Give the extent of all uninfected red blood cells.
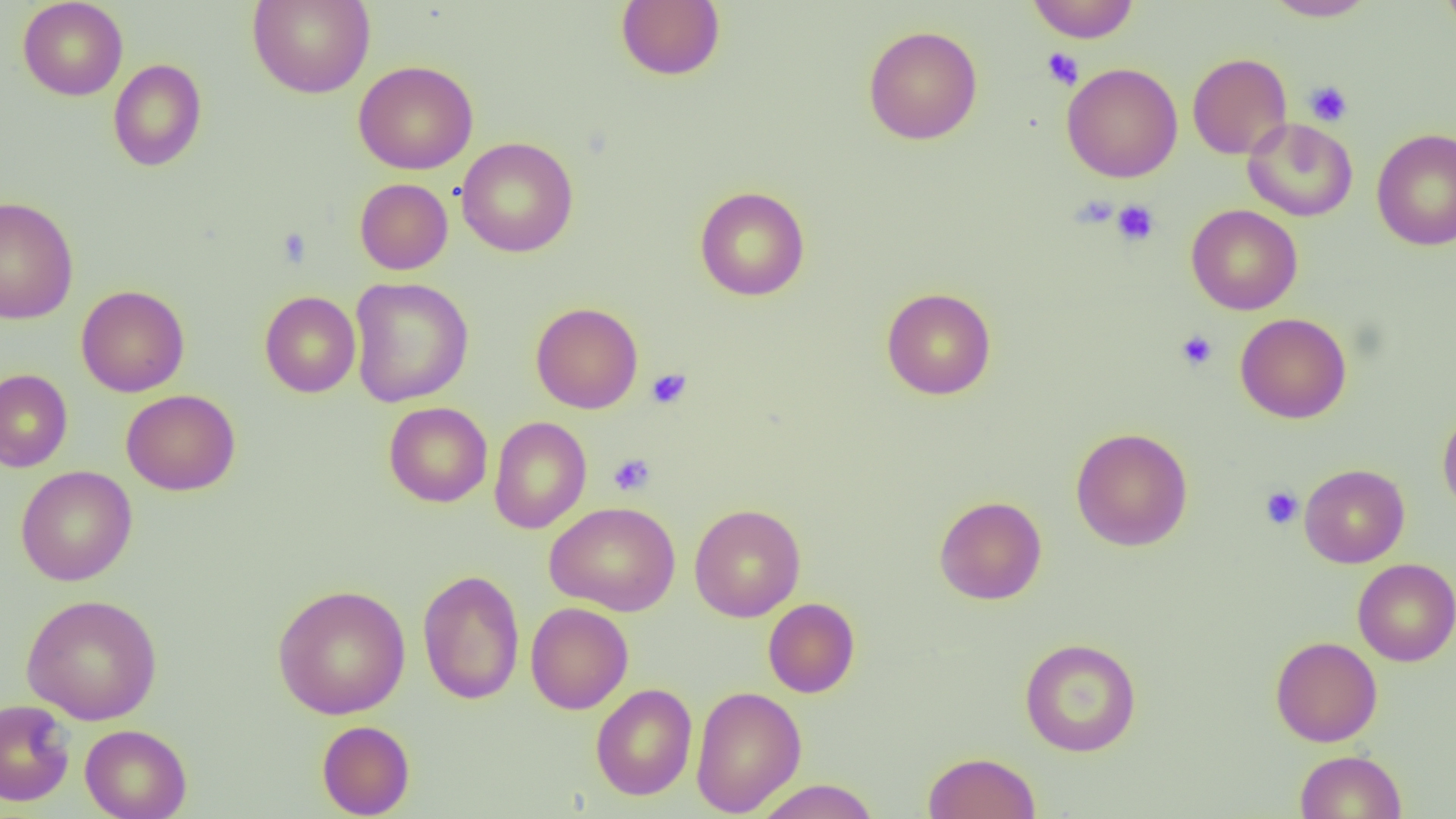

Approximate bounding boxes as (x1, y1, x2, y2) in pixels.
Uninfected red blood cells: (17, 0, 128, 100), (247, 0, 375, 98), (616, 0, 725, 81), (1026, 0, 1141, 43), (1261, 0, 1377, 21), (1437, 0, 1456, 38), (863, 25, 983, 145), (1187, 53, 1292, 159), (108, 59, 207, 171), (354, 60, 478, 174), (1061, 62, 1183, 182), (1243, 118, 1358, 222), (1371, 127, 1456, 251), (456, 137, 579, 258), (354, 178, 453, 274), (695, 186, 810, 301), (0, 196, 79, 324), (1187, 204, 1303, 315), (349, 277, 473, 407), (76, 285, 190, 397), (881, 287, 997, 400), (260, 291, 361, 397), (530, 302, 643, 413), (1236, 313, 1351, 424), (0, 369, 73, 472), (121, 389, 240, 495), (384, 402, 493, 507), (1437, 406, 1456, 518), (489, 415, 591, 534), (1070, 427, 1193, 551), (1299, 463, 1410, 568), (15, 466, 137, 586), (934, 495, 1047, 605), (545, 501, 681, 616), (689, 503, 806, 622), (1352, 559, 1456, 666), (417, 569, 525, 705), (272, 584, 411, 719), (21, 593, 163, 724), (763, 598, 860, 698), (526, 602, 633, 714), (1270, 636, 1383, 747), (1020, 637, 1142, 757), (591, 684, 697, 801), (690, 685, 806, 816), (0, 699, 75, 806), (317, 720, 415, 818), (79, 724, 192, 819), (1295, 750, 1406, 818), (922, 751, 1041, 819), (753, 779, 881, 818).

Platelet locations: (1042, 47, 1084, 89), (1304, 80, 1353, 127), (1113, 200, 1159, 245), (275, 228, 314, 268), (1176, 330, 1218, 371), (646, 368, 692, 409), (608, 453, 656, 496), (1260, 486, 1303, 529). Slide-level diagnosis: negative for blood parasites. One field of a larger specimen. Image is 1456×819 pixels. Light microscopy. 1000x magnification. Thin blood smear.